Classify this cell by malaria status.
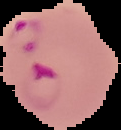
It is parasitized.

Cell region segmented out of the field of view; the surrounding area is masked to black. Image is 121×130 pixels. From a thin blood film.